Locate every leukocyte (white blood cell).
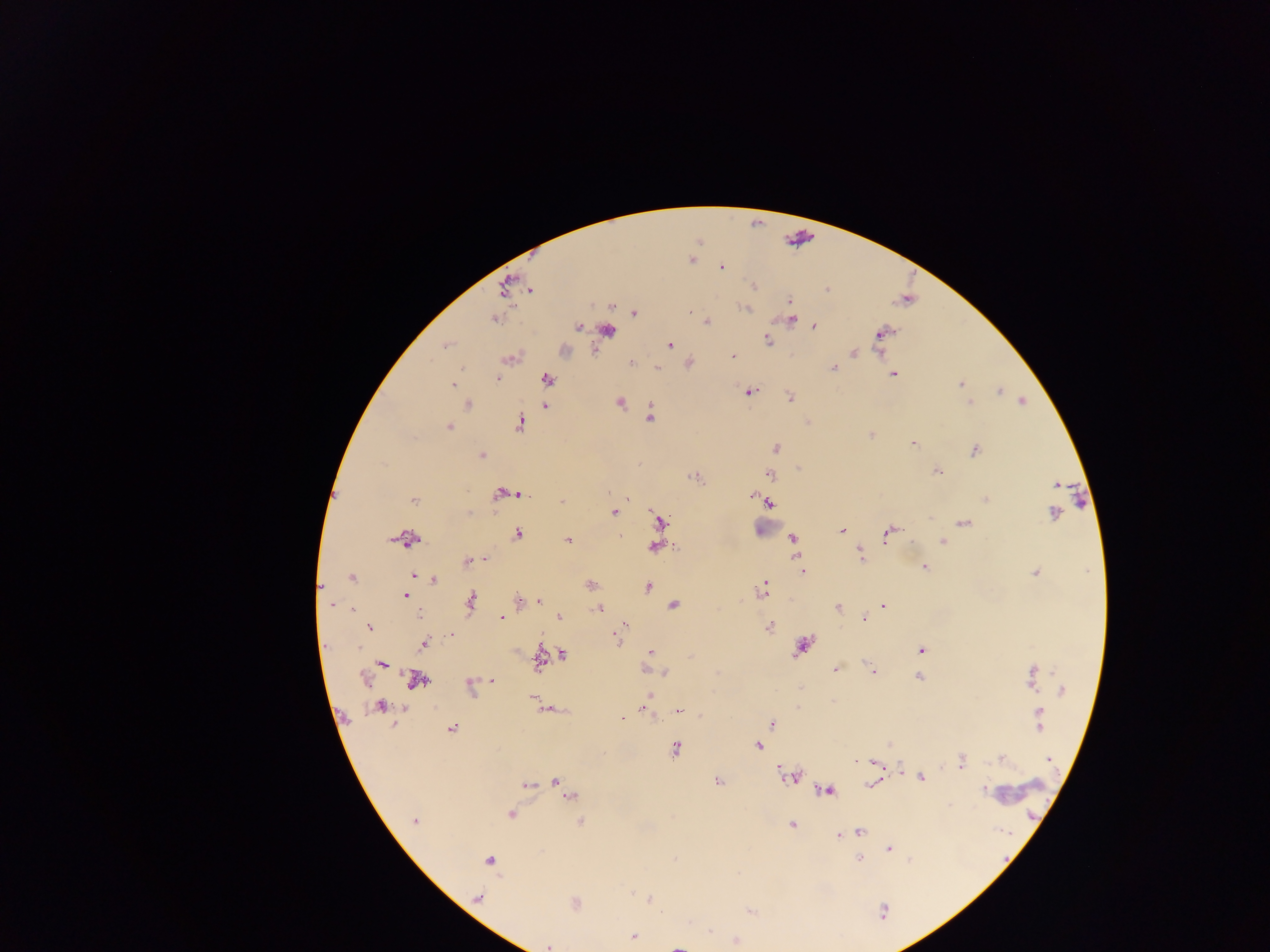

Approximate centers as {x, y} in pixels.
Leukocytes: {765, 526}.

Summary:
  - Plasmodium parasite locations: {692, 260}, {722, 267}, {754, 285}, {504, 287}, {827, 289}, {530, 290}, {789, 301}, {746, 308}, {690, 311}, {634, 313}, {493, 319}, {791, 319}, {706, 321}, {578, 326}, {814, 326}, {608, 330}, {882, 333}, {767, 340}, {669, 345}, {445, 346}, {854, 353}, {733, 356}, {509, 359}, {631, 363}, {658, 367}, {833, 367}, {893, 374}, {496, 379}, {547, 379}, {961, 383}, {453, 385}, {750, 391}, {999, 392}, {790, 397}, {1022, 401}, {619, 402}, {970, 403}, {468, 405}, {545, 406}, {650, 417}, {520, 424}, {448, 427}, {871, 434}, {913, 444}, {775, 448}, {974, 450}, {481, 454}, {798, 468}, {937, 471}, {770, 474}, {695, 478}, {1056, 484}, {499, 494}, {512, 494}, {522, 494}, {750, 495}, {627, 499}, {985, 499}, {414, 500}, {562, 501}, {768, 503}, {615, 513}, {1052, 513}, {661, 521}, {965, 523}, {842, 531}, {517, 534}, {888, 534}, {408, 539}, {793, 539}, {569, 541}, {942, 541}, {911, 542}, {794, 545}, {654, 547}, {861, 554}, {485, 560}, {468, 561}, {924, 568}, {803, 572}, {1035, 572}, {416, 576}, {352, 578}, {434, 580}, {591, 585}, {764, 586}, {321, 587}, {647, 587}, {405, 595}, {518, 599}, {539, 600}, {471, 602}, {331, 605}, {673, 606}, {884, 606}, {597, 608}, {838, 608}, {351, 609}, {419, 615}, {559, 617}, {501, 618}, {865, 618}, {623, 625}, {769, 627}, {369, 628}, {452, 635}, {618, 639}, {423, 644}, {802, 647}, {921, 650}, {650, 653}, {562, 655}, {539, 660}, {382, 664}, {835, 669}, {873, 671}, {665, 673}, {918, 677}, {1033, 677}, {364, 678}, {491, 680}, {416, 681}, {470, 686}, {1062, 690}, {532, 698}, {648, 698}, {833, 701}, {380, 707}, {547, 709}, {644, 709}, {678, 711}, {623, 719}, {1040, 719}, {772, 723}, {451, 729}, {758, 746}, {675, 749}, {1001, 758}, {1049, 760}, {856, 761}, {961, 762}, {790, 776}, {921, 778}, {556, 780}, {717, 781}, {870, 784}, {526, 785}, {562, 787}, {827, 790}, {984, 790}, {570, 797}, {510, 814}, {413, 821}, {581, 822}, {792, 825}, {860, 832}, {838, 836}, {889, 849}, {675, 858}, {859, 859}, {489, 860}, {478, 897}, {649, 898}, {575, 903}, {884, 911}, {634, 937}, {736, 941}, {548, 946}, {677, 947}
  - Country: Ghana
  - Preparation: thick blood film
  - Field of view: single
  - Image size: 1270×952 pixels
  - Capture: mobile-phone photograph through a microscope